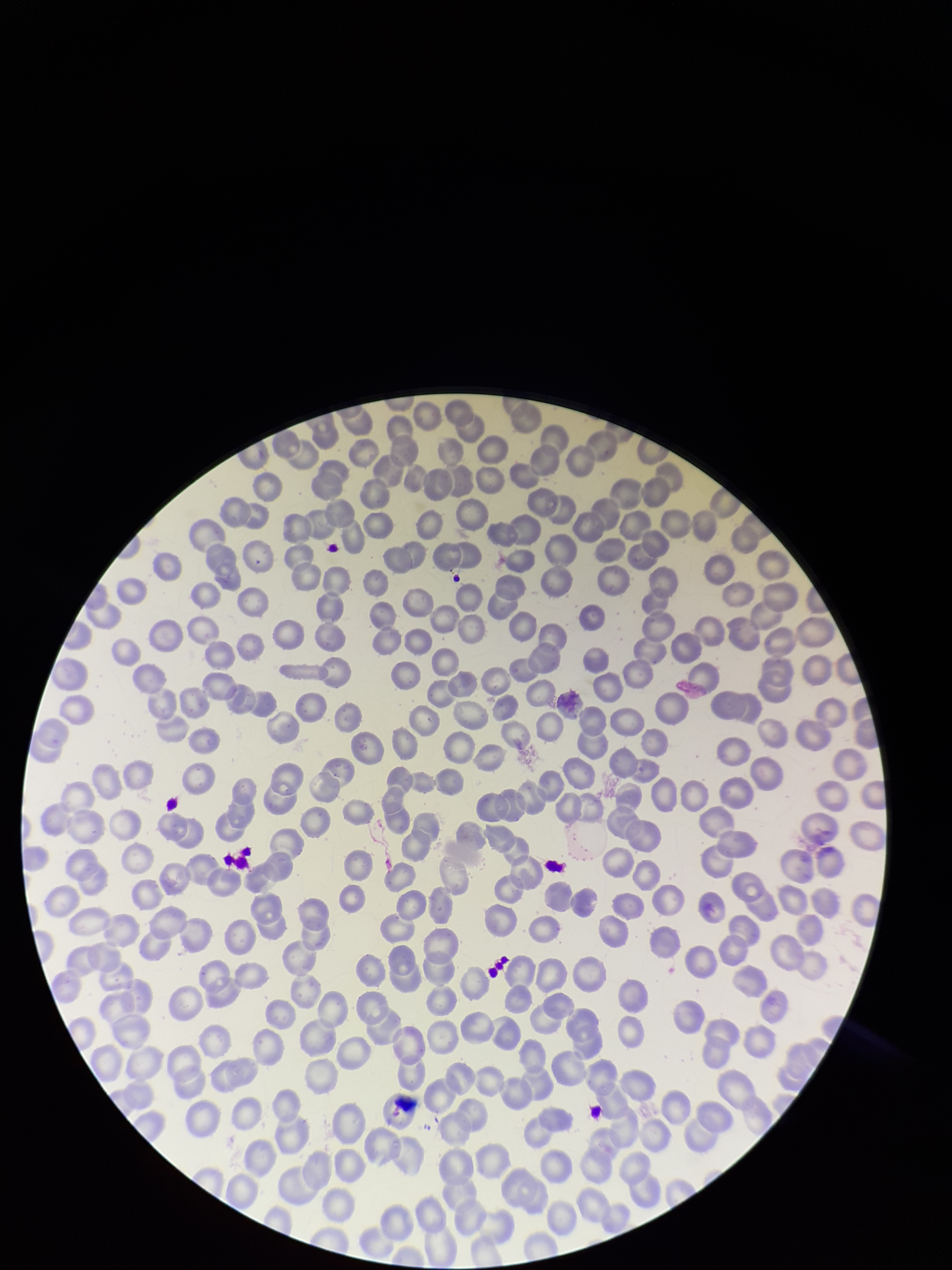 Image is 952×1270 pixels. Parasitized red blood cell count: 0. Red blood cell count: 266. Preparation: thin blood smear. Patient malaria status: negative. One field from this slide. Smartphone photograph taken through the eyepiece of a microscope. Stained with Giemsa. Parasitized red blood cells: none identified.